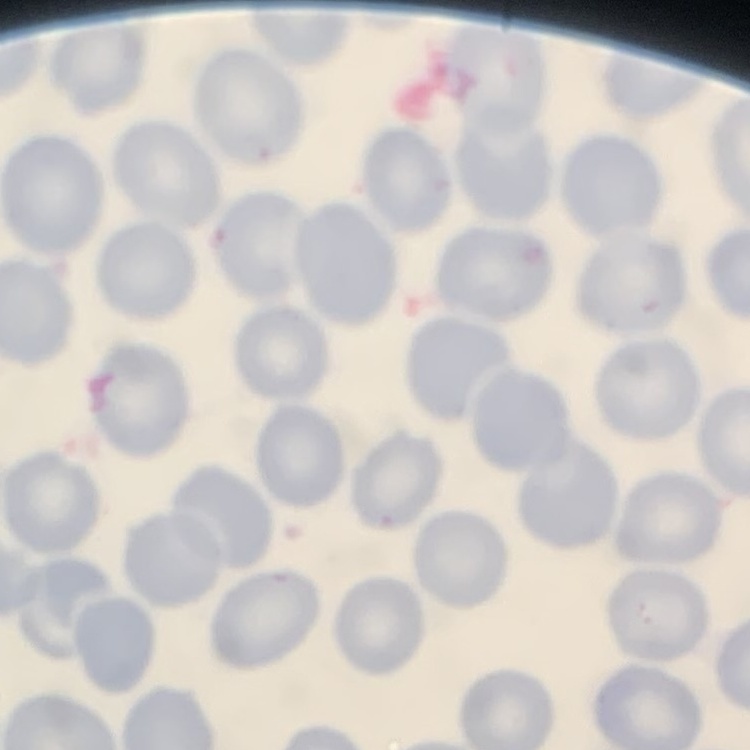

{
  "red_blood_cell_morphology": "no rouleaux formation",
  "stain": "Field's or Giemsa",
  "preparation": "thin blood smear",
  "image_type": "square crop of a larger photomicrograph"
}